Describe the morphology of the erythrocytes.
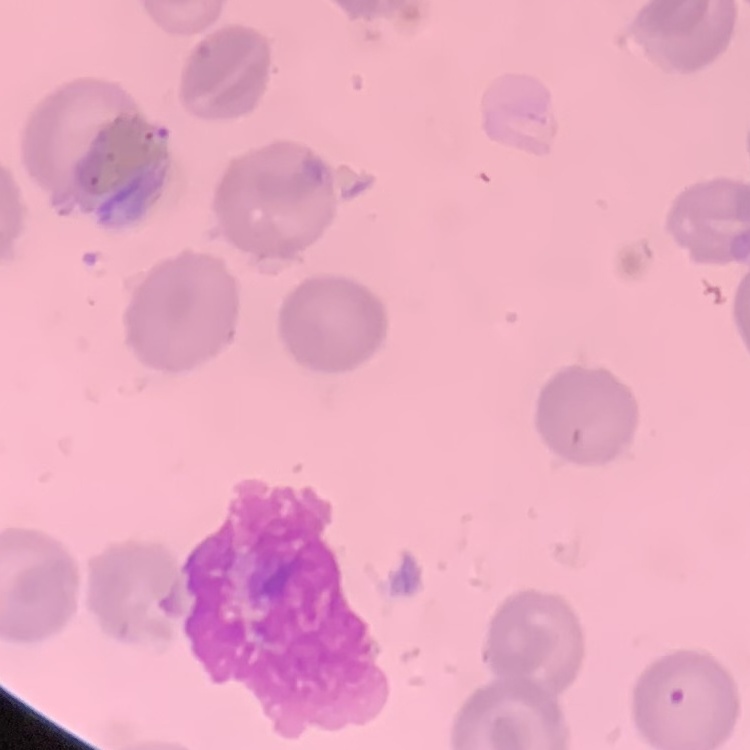

No rouleaux formation.

preparation: thin blood smear
image_type: square crop of a larger photomicrograph
stain: Field's or Giemsa